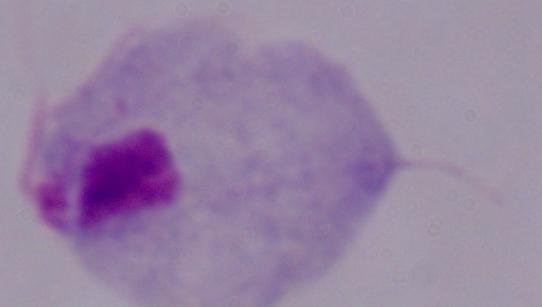

1000x magnification. A trichomonad is seen. Micrograph.